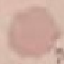

Result: negative for malaria parasites. Thin smear of blood. Cell patch, automatically extracted from a larger field of view and resized to 64 × 64 pixels. Photographed with a smartphone camera at the microscope eyepiece. Giemsa-stained preparation.